Assess the morphology of the erythrocytes.
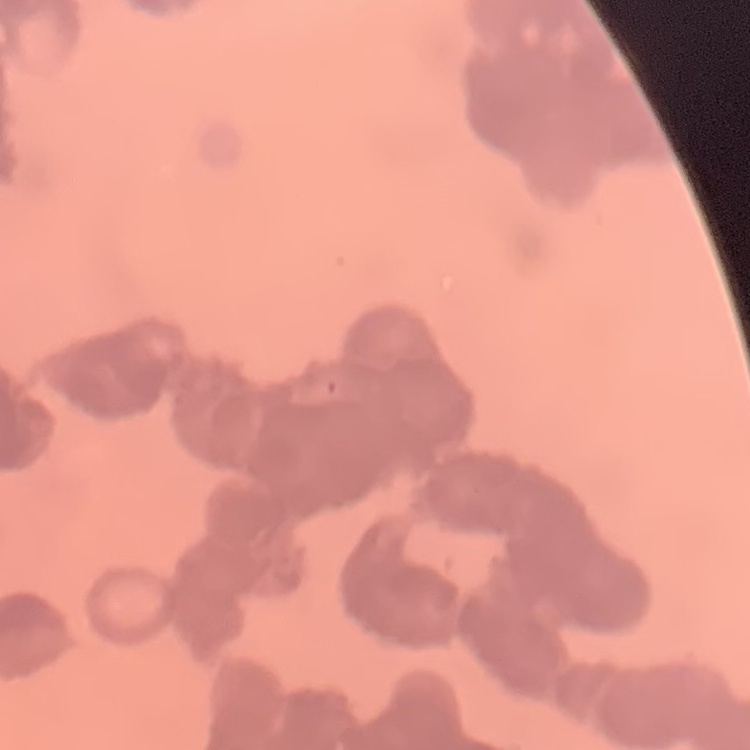
They show rouleaux formation.

Thin blood film. Square crop of a larger photomicrograph. Field's or Giemsa stain.